State which parasite is depicted.
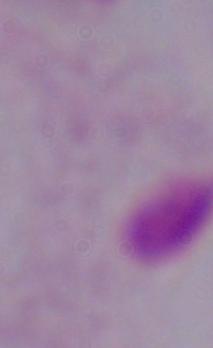
This is a trichomonad.

Captured at 1000x magnification. Photomicrograph.